Assess this cell for malaria.
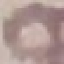
It is uninfected.

Summary:
  - Preparation: thin blood film
  - Stain: Giemsa
  - Image type: cell patch, automatically extracted from a larger field of view and resized to 64 × 64 pixels
  - Capture: smartphone camera at the microscope eyepiece